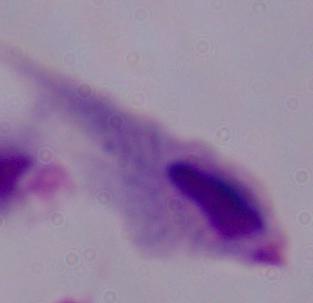

1000x magnification. Photomicrograph. A trichomonad is shown.